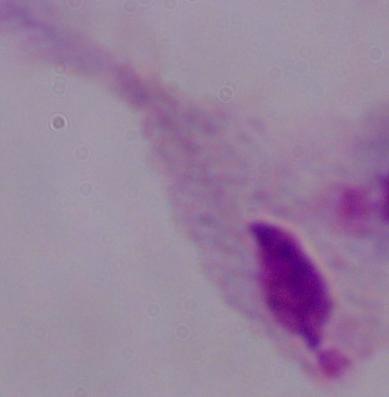

Summary:
  - Magnification: 1000x
  - Identification: trichomonad
  - Modality: photomicrograph